State which parasite is depicted.
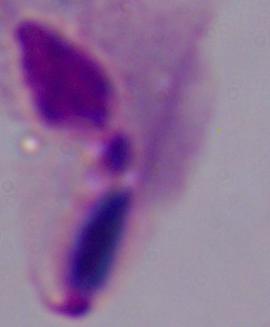
A trichomonad.

magnification = 1000x
modality = micrograph